Classify this cell by malaria status.
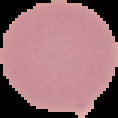
It is uninfected.

Image is 118×118 pixels. The area outside the segmented cell region is set to black. From a thin blood film.